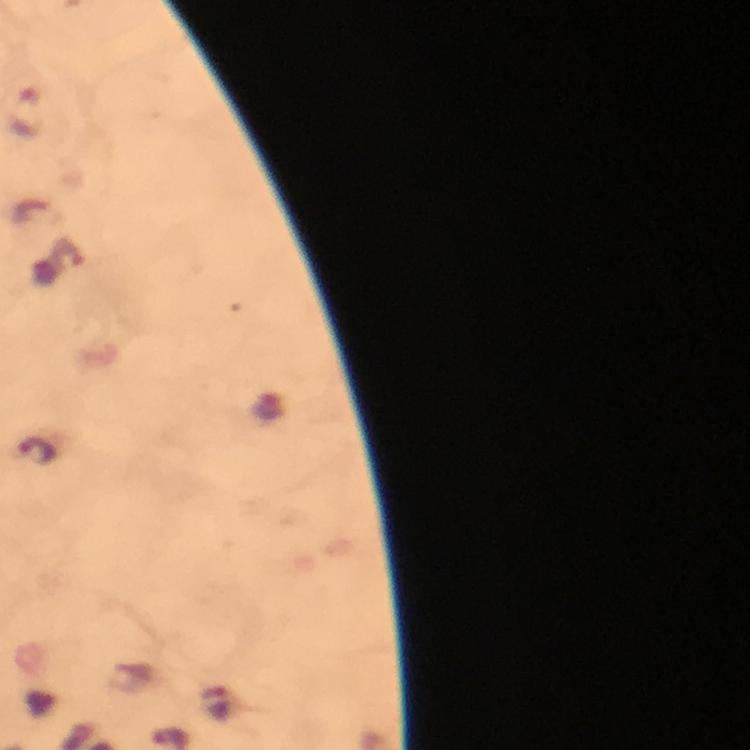
{
  "preparation": "thick smear",
  "stain": "Giemsa",
  "image_size": "750×750 pixels",
  "plasmodium_parasite_locations": "approximate centers as (x, y) in pixels: (24, 114), (68, 253), (38, 452), (222, 705)",
  "cropped_from": "one field of view",
  "capture": "smartphone camera through the microscope",
  "magnification": "100x",
  "immersion_oil": "used",
  "context": "from a malaria diagnostic workup"
}